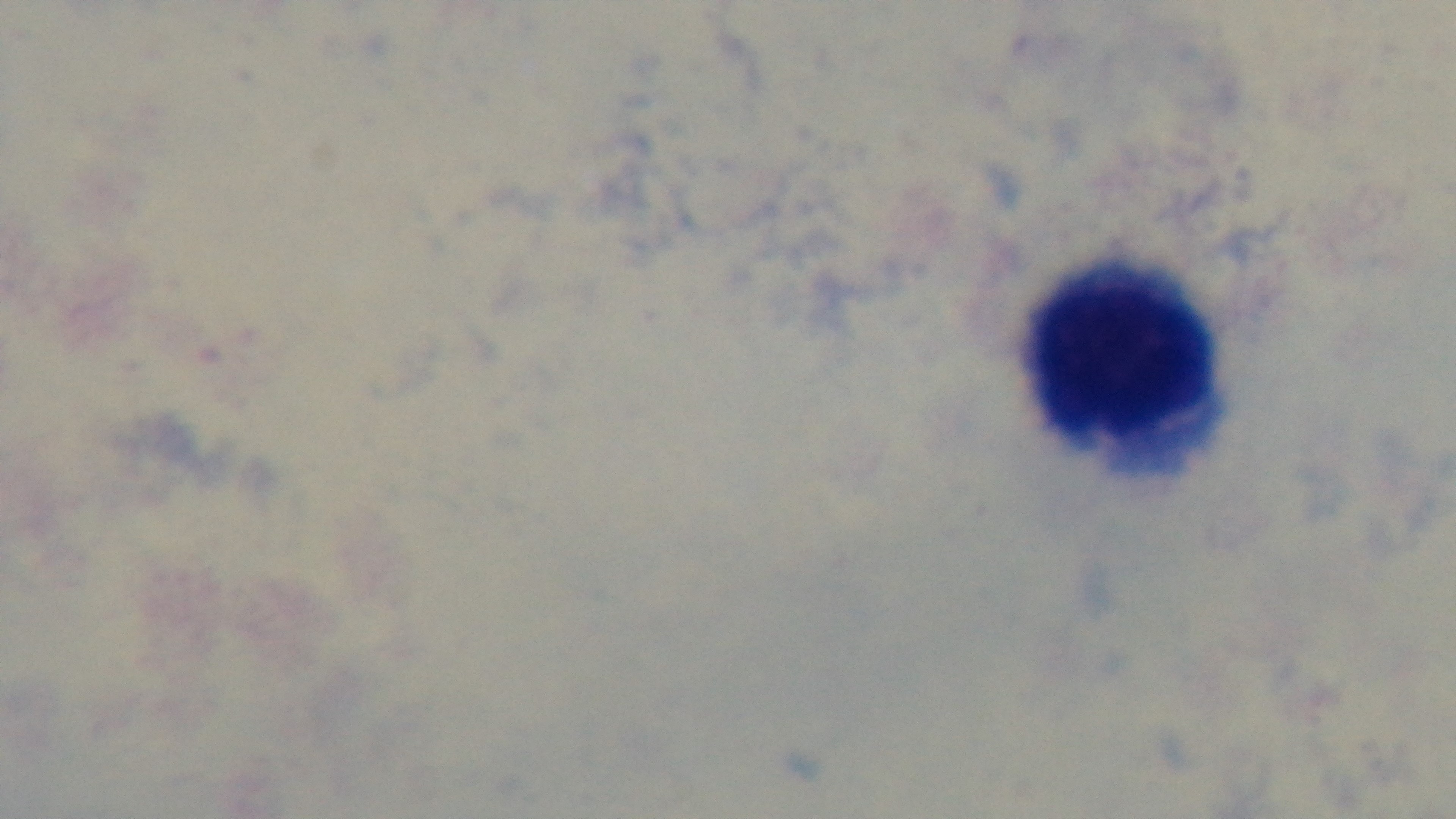

Summary:
  - Preparation: thick blood film
  - Field of view: one from the slide
  - Objective: 100x oil immersion
  - Malaria status: uninfected
  - Stain: Giemsa
  - Capture: mounted 4K digital camera
  - Modality: light microscopy